State which parasite is depicted.
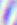

Toxoplasma gondii.

Photomicrograph. Captured at 400x magnification.